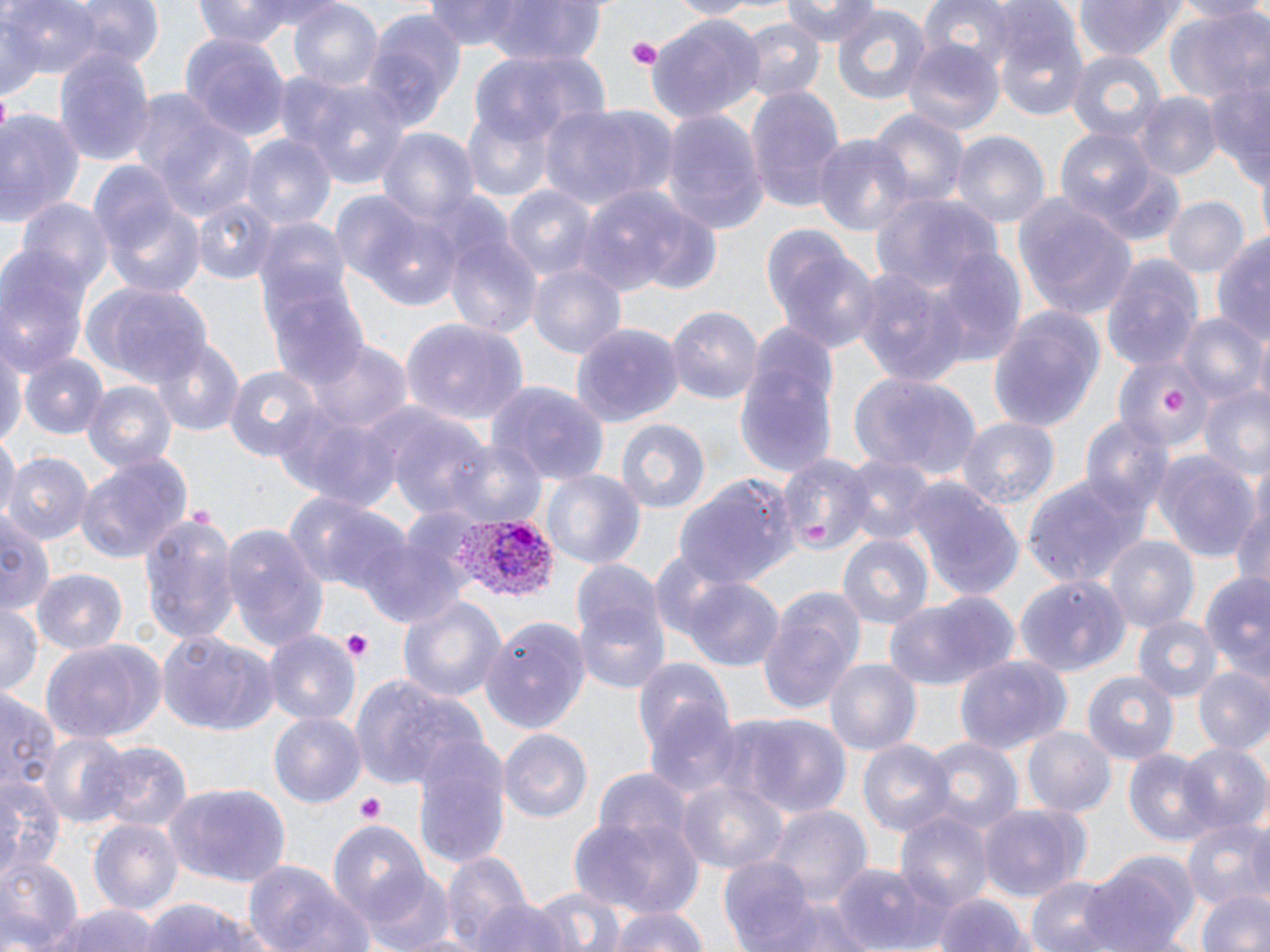

Summary:
  - Coordinate format: approximate bounding boxes as [x1, y1, x2, y2] in pixels
  - Uninfected red blood cell locations: [63, 0, 165, 70], [189, 0, 315, 46], [475, 0, 609, 63], [665, 0, 756, 17], [784, 0, 879, 46], [915, 0, 1019, 71], [1074, 0, 1185, 61], [1167, 0, 1270, 22], [7, 1, 104, 84], [289, 1, 385, 93], [422, 2, 538, 52], [830, 5, 932, 106], [989, 6, 1089, 123], [362, 8, 465, 123], [1164, 9, 1270, 107], [647, 16, 765, 122], [735, 16, 825, 102], [180, 31, 289, 143], [900, 38, 1005, 137], [54, 44, 156, 171], [1064, 47, 1166, 143], [472, 48, 609, 151], [1200, 62, 1270, 179], [294, 79, 416, 193], [745, 87, 846, 211], [1135, 94, 1220, 180], [541, 100, 677, 212], [145, 104, 260, 225], [865, 106, 969, 209], [0, 107, 88, 232], [460, 107, 554, 202], [660, 109, 769, 233], [1054, 124, 1161, 228], [376, 129, 476, 227], [813, 132, 914, 239], [950, 132, 1050, 228], [244, 135, 335, 231], [91, 169, 205, 297], [580, 185, 720, 300], [503, 186, 596, 285], [334, 188, 460, 311], [869, 191, 1002, 295], [1013, 195, 1139, 322], [1162, 195, 1250, 279], [192, 198, 277, 285], [20, 199, 113, 297], [440, 219, 543, 339], [762, 227, 878, 354], [1213, 231, 1270, 352], [0, 247, 92, 375], [928, 250, 1025, 365], [1101, 252, 1203, 371], [528, 262, 625, 361], [849, 266, 969, 389], [83, 282, 213, 388], [266, 286, 371, 393], [669, 304, 763, 406], [986, 304, 1105, 431], [1177, 314, 1265, 406], [399, 317, 530, 424], [573, 322, 682, 425], [736, 327, 839, 486], [0, 340, 26, 446], [153, 340, 244, 436], [307, 340, 410, 431], [1114, 351, 1215, 455], [19, 354, 108, 442], [225, 363, 327, 463], [847, 371, 981, 482], [81, 379, 178, 472], [488, 381, 611, 487], [1196, 385, 1270, 479], [273, 405, 403, 510], [385, 413, 496, 526], [1080, 414, 1172, 520], [956, 416, 1060, 510], [612, 418, 709, 515], [1, 434, 17, 522], [441, 439, 548, 531], [1154, 451, 1259, 563], [3, 452, 91, 546], [75, 452, 193, 563], [778, 452, 870, 555], [838, 454, 936, 546], [541, 468, 645, 574], [675, 473, 799, 588], [1022, 473, 1151, 588], [907, 483, 1025, 600], [284, 488, 411, 600], [1230, 500, 1270, 596], [135, 509, 242, 649], [0, 511, 54, 618], [220, 524, 330, 651], [358, 533, 465, 629], [836, 534, 935, 633], [1103, 537, 1199, 636], [569, 558, 663, 660], [36, 568, 128, 656], [1198, 572, 1270, 681], [1017, 573, 1130, 675], [678, 576, 785, 670], [757, 588, 865, 714], [574, 591, 672, 696], [883, 591, 1019, 692], [396, 593, 506, 705], [0, 600, 42, 699], [1131, 614, 1222, 704], [481, 616, 591, 736], [156, 630, 278, 736], [264, 630, 361, 730], [37, 639, 163, 744], [635, 654, 739, 787], [954, 654, 1070, 754], [825, 658, 922, 756], [1193, 667, 1270, 755], [345, 671, 476, 793], [1084, 671, 1180, 764], [0, 687, 58, 803], [267, 711, 368, 808], [726, 712, 849, 819], [1024, 728, 1115, 815], [498, 729, 594, 823], [37, 730, 135, 829], [413, 735, 511, 869], [858, 739, 954, 839], [923, 739, 1022, 837], [89, 741, 192, 834], [1177, 741, 1268, 835], [1123, 749, 1217, 846], [593, 768, 692, 855], [0, 777, 59, 881], [676, 777, 789, 876], [169, 784, 291, 891], [980, 803, 1089, 897], [768, 806, 870, 905], [896, 811, 993, 912], [569, 814, 703, 917], [1182, 817, 1270, 914], [88, 819, 183, 920], [328, 819, 434, 927], [441, 852, 534, 952], [0, 853, 84, 951], [1082, 853, 1196, 952], [718, 856, 818, 949], [833, 859, 951, 952], [243, 862, 372, 952], [359, 868, 459, 952], [1025, 874, 1123, 952], [528, 886, 631, 952], [1196, 888, 1270, 952], [935, 893, 1035, 952], [137, 898, 278, 952], [764, 899, 872, 952], [466, 900, 574, 952], [39, 901, 169, 952], [605, 902, 706, 952]
  - Platelet locations: [625, 36, 663, 70], [1162, 388, 1188, 417], [802, 519, 832, 544], [341, 630, 375, 659], [354, 796, 385, 824]
  - Plasmodium vivax-infected red blood cell locations: [452, 511, 559, 607]
  - Slide-level diagnosis: Plasmodium vivax
  - Modality: light microscopy
  - Field of view: single
  - Stain: May-Grünwald-Giemsa
  - Preparation: thin blood film
  - Image size: 1270×952 pixels
  - Magnification: 1000x